Locate every blood parasite and identify its species.
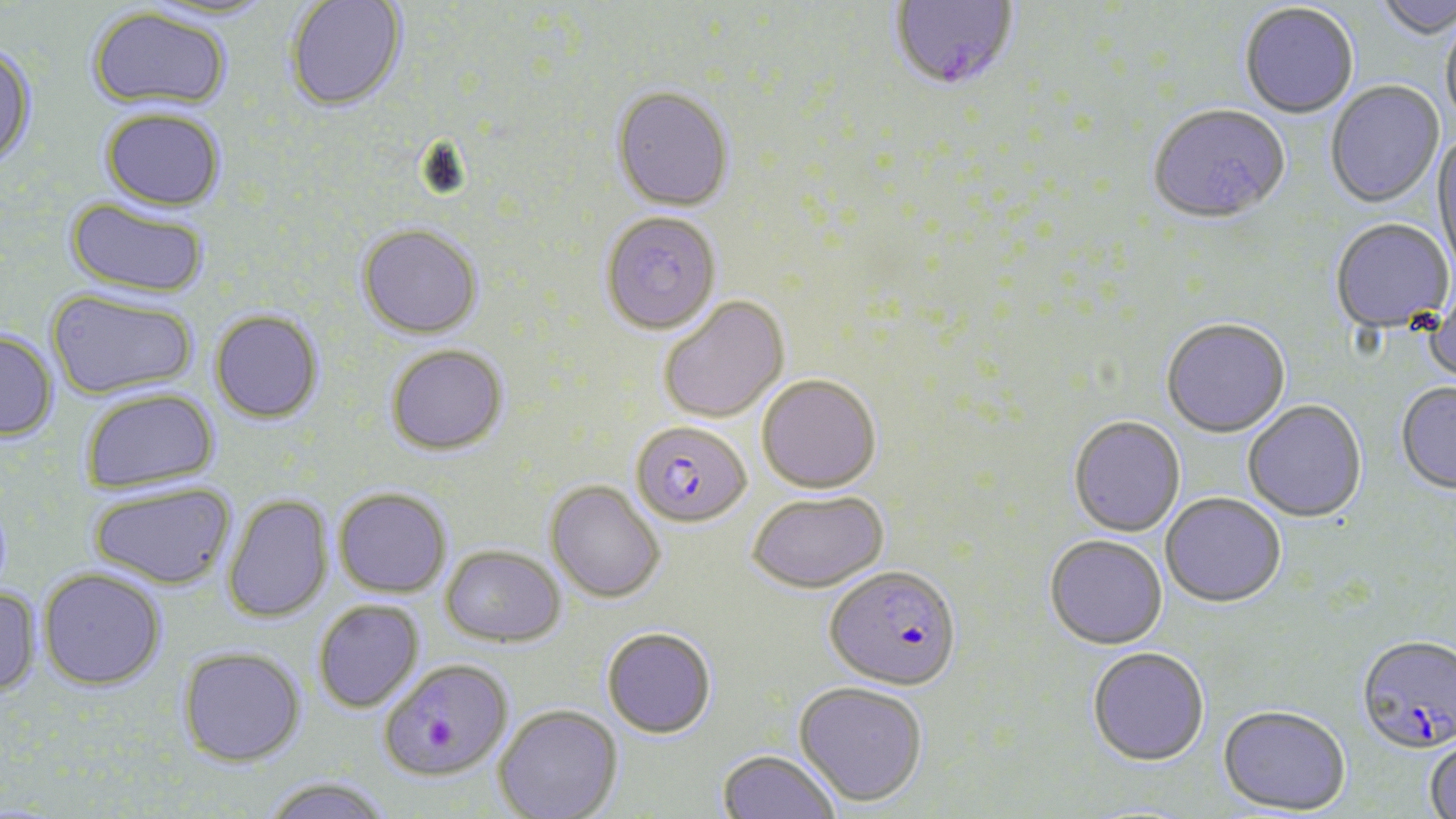
Approximate bounding boxes as named x1/y1/x2/y2 corners in pixels.
Plasmodium falciparum-infected red blood cells: (x1=890, y1=0, x2=1019, y2=93), (x1=630, y1=420, x2=752, y2=527), (x1=824, y1=566, x2=962, y2=693), (x1=1356, y1=637, x2=1456, y2=757), (x1=379, y1=659, x2=513, y2=781).
No Plasmodium ovale, Plasmodium malariae, Plasmodium vivax, Babesia divergens, or Trypanosoma brucei observed.

slide-level diagnosis = Plasmodium falciparum
image size = 1456×819 pixels
uninfected red blood cell locations = approximate bounding boxes as named x1/y1/x2/y2 corners in pixels: (x1=1372, y1=0, x2=1456, y2=42), (x1=284, y1=1, x2=407, y2=112), (x1=1240, y1=4, x2=1358, y2=120), (x1=87, y1=6, x2=232, y2=112), (x1=1441, y1=17, x2=1456, y2=133), (x1=0, y1=44, x2=37, y2=169), (x1=1326, y1=82, x2=1444, y2=209), (x1=611, y1=86, x2=734, y2=211), (x1=100, y1=107, x2=226, y2=211), (x1=1148, y1=107, x2=1290, y2=227), (x1=1432, y1=133, x2=1456, y2=276), (x1=66, y1=195, x2=210, y2=299), (x1=599, y1=212, x2=722, y2=335), (x1=1330, y1=220, x2=1454, y2=334), (x1=356, y1=223, x2=484, y2=339), (x1=1423, y1=285, x2=1456, y2=392), (x1=46, y1=288, x2=199, y2=400), (x1=659, y1=296, x2=789, y2=424), (x1=210, y1=309, x2=324, y2=424), (x1=1161, y1=321, x2=1291, y2=440), (x1=0, y1=330, x2=59, y2=442), (x1=386, y1=344, x2=509, y2=454), (x1=757, y1=374, x2=881, y2=493), (x1=1396, y1=384, x2=1456, y2=495), (x1=80, y1=388, x2=221, y2=493), (x1=1243, y1=401, x2=1367, y2=525), (x1=1068, y1=417, x2=1185, y2=538), (x1=545, y1=481, x2=665, y2=603), (x1=88, y1=482, x2=237, y2=589), (x1=334, y1=487, x2=452, y2=597), (x1=747, y1=490, x2=889, y2=594), (x1=222, y1=494, x2=333, y2=624), (x1=1160, y1=495, x2=1286, y2=610), (x1=1044, y1=537, x2=1168, y2=652), (x1=441, y1=544, x2=566, y2=647), (x1=38, y1=567, x2=167, y2=690), (x1=0, y1=584, x2=41, y2=699), (x1=313, y1=599, x2=425, y2=713), (x1=602, y1=626, x2=716, y2=738), (x1=177, y1=646, x2=306, y2=767), (x1=1087, y1=649, x2=1209, y2=768), (x1=794, y1=681, x2=928, y2=807), (x1=493, y1=705, x2=622, y2=819), (x1=1217, y1=708, x2=1350, y2=817), (x1=1425, y1=736, x2=1456, y2=819), (x1=716, y1=749, x2=840, y2=818), (x1=261, y1=776, x2=394, y2=819)
preparation = thin blood smear
modality = optical microscopy
stain = May-Grünwald-Giemsa
field of view = single
magnification = 1000x